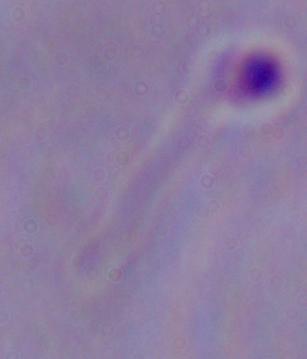
{
  "magnification": "1000x",
  "modality": "micrograph",
  "identification": "Leishmania"
}